Give the position of every leukocyte visible.
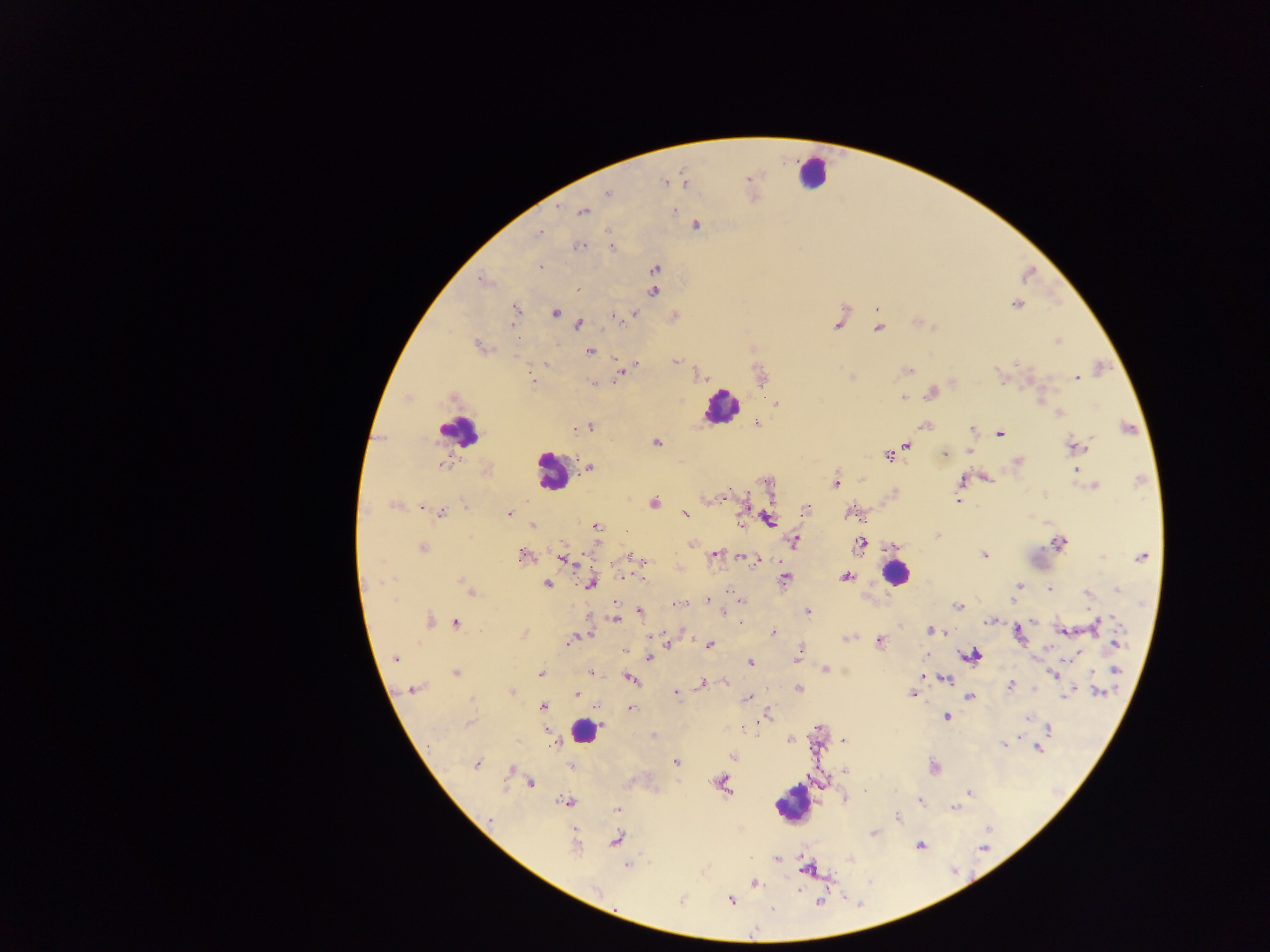

Approximate centers as x y in pixels.
Leukocytes: 812 173; 721 407; 458 430; 552 471; 894 573; 583 731; 791 804.

country: Ghana
plasmodium_parasite_locations: 'approximate centers as x y in pixels: 749 178; 664 183; 608 193; 673 210; 583 212; 696 225; 608 231; 540 232; 579 247; 612 248; 540 267; 655 269; 480 280; 577 289; 654 292; 1016 304; 515 307; 877 309; 554 313; 634 313; 613 316; 837 323; 512 324; 579 324; 878 328; 1057 341; 479 346; 590 352; 675 362; 635 363; 626 370; 907 370; 621 375; 1077 377; 533 381; 592 383; 931 393; 453 397; 902 398; 1040 398; 774 403; 1060 412; 757 423; 923 426; 590 428; 576 429; 972 429; 1000 433; 656 443; 907 445; 1075 446; 969 451; 945 453; 888 456; 1018 461; 443 465; 589 468; 1077 469; 986 479; 963 481; 836 482; 1095 486; 957 501; 654 502; 394 506; 465 506; 422 507; 806 509; 441 512; 850 513; 509 514; 685 514; 741 519; 769 519; 533 526; 597 527; 938 536; 793 540; 860 543; 691 544; 1059 544; 422 548; 715 554; 523 555; 984 556; 631 557; 1142 557; 747 558; 565 559; 640 559; 756 560; 623 576; 846 576; 784 579; 463 581; 592 582; 547 584; 1019 585; 1050 589; 1118 590; 471 592; 1087 594; 740 599; 708 600; 394 601; 678 603; 958 606; 808 611; 641 612; 724 613; 615 618; 430 620; 990 620; 456 623; 1095 625; 1062 630; 931 631; 773 632; 1019 634; 846 638; 572 640; 879 641; 1116 643; 710 646; 625 650; 799 652; 1076 654; 972 655; 395 658; 649 658; 749 663; 825 669; 1116 670; 590 672; 456 673; 541 674; 923 675; 1054 675; 630 678; 945 680; 726 682; 702 683; 1011 685; 798 688; 412 689; 512 691; 679 691; 676 692; 1098 692; 912 694; 576 695; 1065 696; 969 697; 747 698; 593 706; 543 707; 629 707; 767 715; 947 716; 1028 718; 468 723; 742 729; 1049 729; 654 735; 789 740; 843 741; 1005 745; 1038 748; 733 756; 677 763; 477 764; 571 767; 934 767; 510 769; 845 771; 721 783; 531 784; 895 792; 969 792; 845 799; 920 801; 567 802; 953 807; 617 809; 897 818; 491 819; 616 839; 575 844; 921 845; 984 848; 777 859; 627 866; 808 868; 755 883; 596 890; 730 900; 681 902; 819 903; 772 909'
capture: mobile-phone photograph through a microscope
field_of_view: single
preparation: thick blood film
image_size: 1270×952 pixels